Identify the cell.
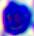
This is a leukocyte.

modality = photomicrograph
magnification = 400x